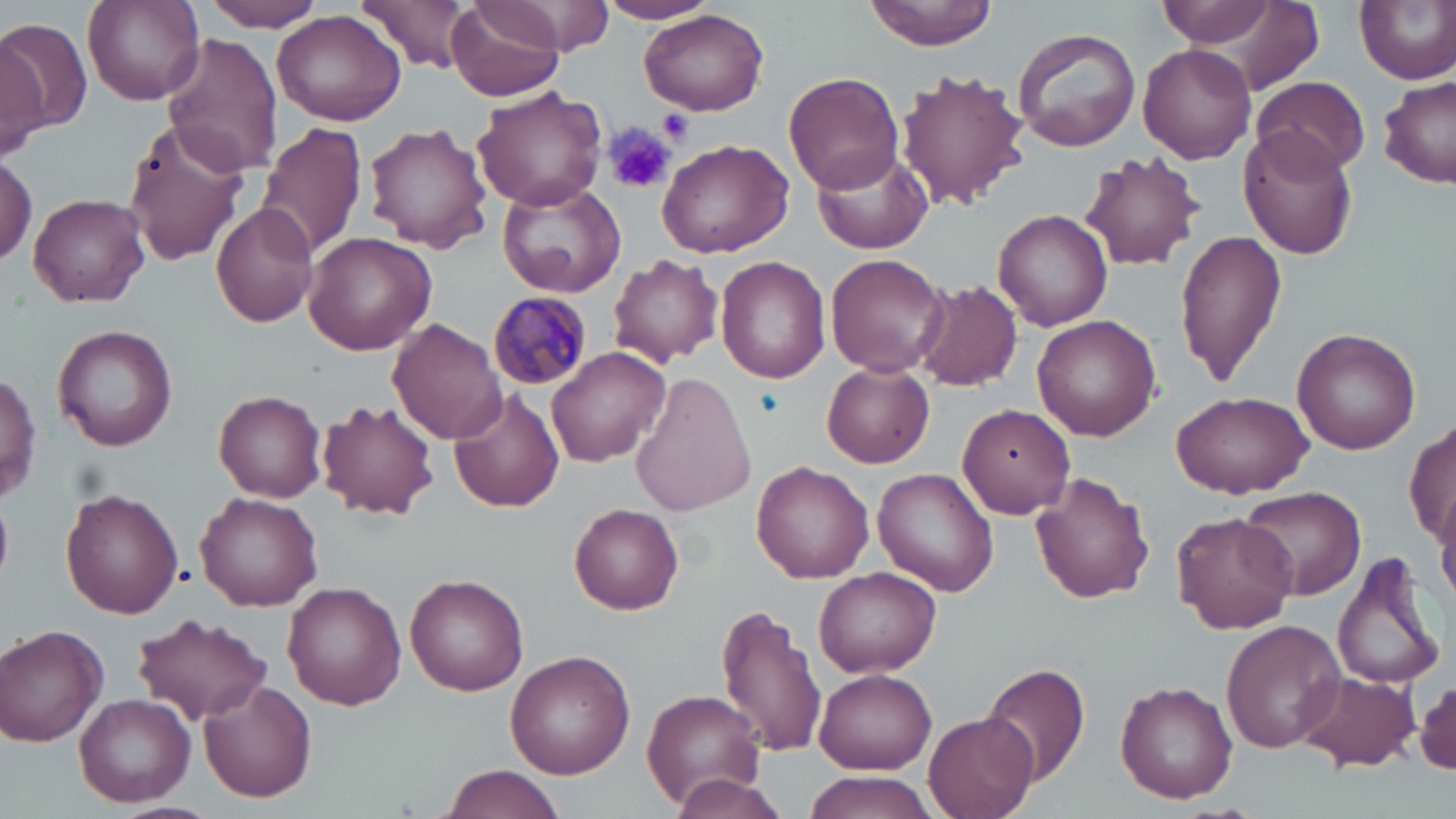

{
  "slide_level_diagnosis": "Plasmodium malariae",
  "image_size": "1456×819 pixels",
  "platelet_locations": "approximate bounding boxes as [x1, y1, x2, y2] in pixels: [657, 106, 694, 145], [602, 126, 675, 195]",
  "modality": "light microscopy",
  "field_of_view": "single",
  "uninfected_red_blood_cell_locations": "approximate bounding boxes as [x1, y1, x2, y2] in pixels: [82, 0, 202, 107], [205, 0, 326, 31], [355, 0, 480, 73], [599, 0, 719, 25], [865, 0, 997, 51], [1157, 0, 1319, 90], [1162, 0, 1281, 49], [1353, 0, 1456, 84], [447, 2, 565, 101], [465, 3, 571, 56], [639, 8, 770, 115], [271, 9, 409, 127], [0, 15, 92, 138], [1012, 26, 1142, 153], [0, 31, 53, 161], [162, 33, 285, 179], [1139, 44, 1256, 163], [896, 69, 1028, 212], [786, 70, 903, 194], [1378, 74, 1455, 189], [1251, 77, 1371, 175], [471, 86, 609, 212], [121, 117, 253, 266], [258, 120, 368, 258], [364, 122, 492, 252], [1239, 129, 1358, 260], [655, 138, 793, 258], [812, 146, 933, 254], [1079, 151, 1204, 271], [0, 154, 38, 265], [495, 180, 626, 296], [29, 193, 150, 306], [210, 202, 319, 329], [993, 208, 1112, 330], [1174, 230, 1288, 387], [304, 231, 435, 354], [825, 253, 949, 377], [608, 255, 722, 366], [714, 257, 830, 384], [912, 281, 1022, 391], [1032, 314, 1163, 440], [388, 317, 507, 444], [52, 324, 179, 450], [1291, 327, 1421, 455], [546, 345, 674, 467], [821, 362, 935, 469], [1, 369, 42, 506], [628, 373, 756, 516], [447, 386, 566, 513], [1170, 390, 1313, 496], [214, 391, 327, 502], [316, 399, 439, 520], [957, 404, 1076, 518], [1404, 417, 1456, 554], [906, 422, 1037, 551], [751, 460, 874, 583], [874, 468, 998, 595], [1031, 471, 1156, 604], [1435, 480, 1456, 607], [1240, 485, 1367, 602], [59, 488, 183, 619], [195, 492, 323, 610], [568, 503, 684, 616], [1171, 511, 1298, 633], [1331, 547, 1448, 692], [814, 567, 941, 678], [405, 574, 529, 695], [283, 581, 406, 710], [716, 602, 830, 760], [132, 613, 272, 725], [1221, 620, 1345, 754], [0, 625, 108, 748], [505, 649, 635, 779], [980, 662, 1089, 790], [815, 669, 935, 774], [1296, 669, 1420, 772], [200, 677, 317, 802], [1414, 677, 1455, 778], [1116, 682, 1237, 804], [642, 690, 764, 805], [75, 692, 196, 806], [924, 712, 1039, 819], [441, 765, 565, 819], [669, 772, 790, 819], [800, 773, 937, 818]",
  "plasmodium_malariae_infected_red_blood_cell_locations": "approximate bounding boxes as [x1, y1, x2, y2] in pixels: [487, 290, 590, 393]",
  "preparation": "thin blood film",
  "stain": "May-Grünwald-Giemsa",
  "magnification": "1000x"
}